Assess this cell for malaria.
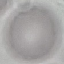

It is uninfected.

Summary:
  - Capture: smartphone camera at the microscope eyepiece
  - Image type: cell patch, automatically extracted from a larger field of view and resized to 64 × 64 pixels
  - Stain: Giemsa
  - Preparation: thin smear